Name the cell type shown.
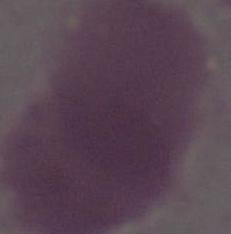
This is an erythrocyte.

Summary:
  - Magnification: 1000x
  - Modality: micrograph